Classify this cell by malaria status.
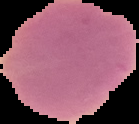
Uninfected.

Summary:
  - Preparation: thin blood smear
  - Image size: 139×124 pixels
  - Image type: cell region segmented out of the field of view; surrounding area masked to black